Classify this cell by malaria status.
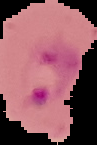
Parasitized.

Cell region segmented out of the field of view; the surrounding area is masked to black. From a thin blood smear. Image is 97×145 pixels.